Name the parasite shown.
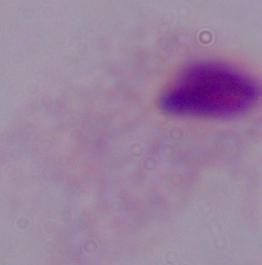

A trichomonad.

Summary:
  - Modality: micrograph
  - Magnification: 1000x